State which parasite is depicted.
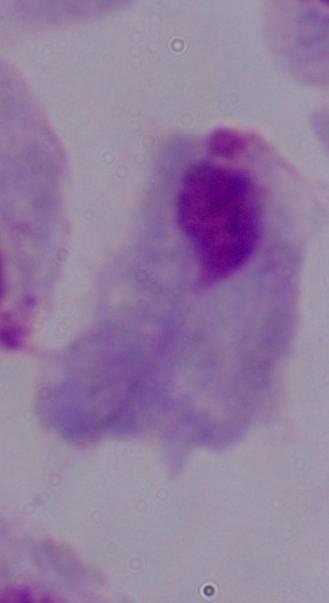

A trichomonad.

1000x magnification. Micrograph.